Locate every malaria parasite and every leukocyte.
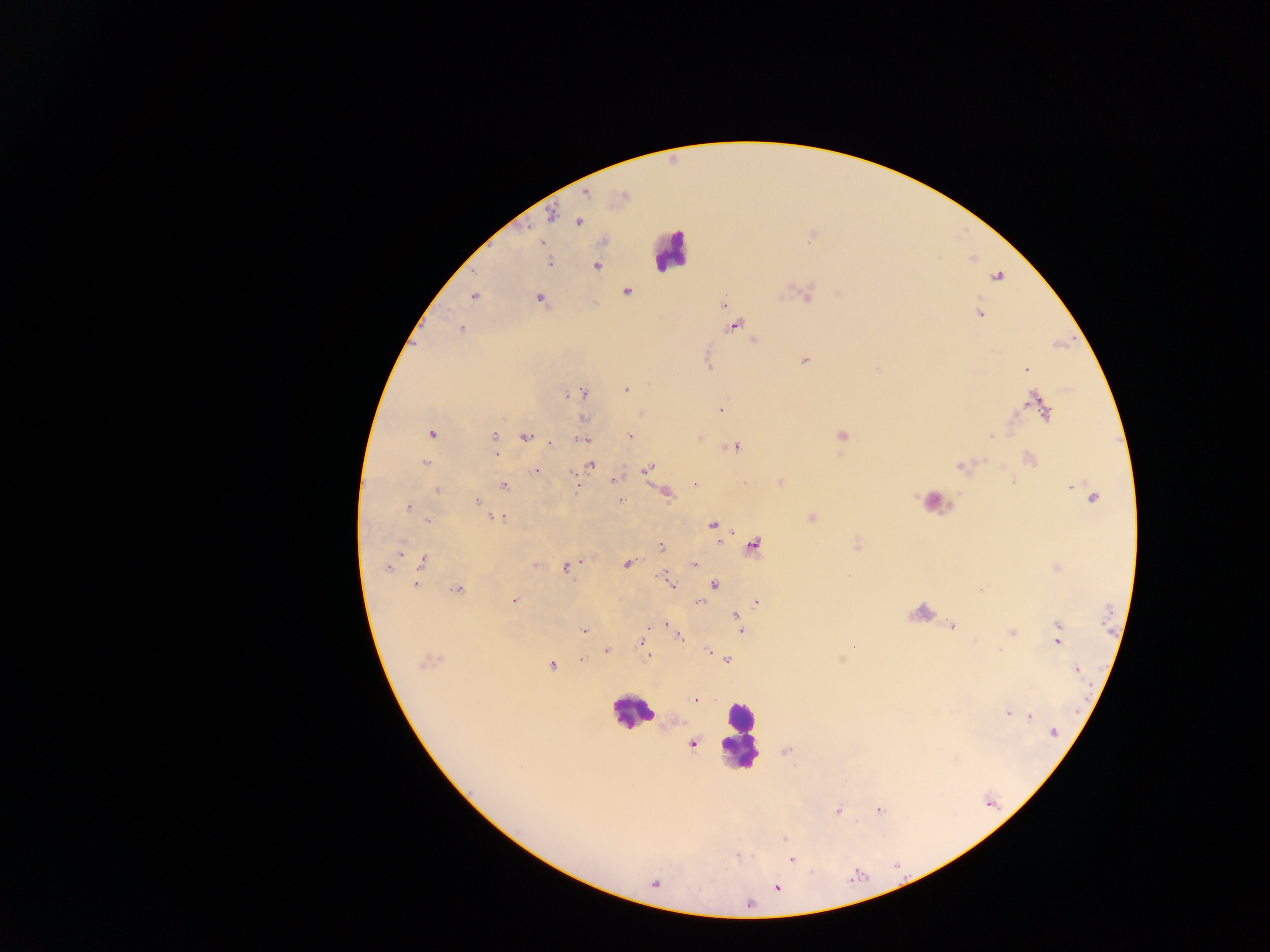

Approximate centers as [x, y] in pixels.
Malaria parasites: [585, 193], [621, 195], [550, 215], [578, 221], [812, 234], [541, 241], [549, 263], [595, 265], [997, 276], [626, 291], [806, 293], [473, 295], [539, 299], [723, 304], [728, 312], [978, 313], [734, 325], [461, 328], [753, 340], [804, 361], [709, 364], [1027, 369], [625, 390], [583, 392], [569, 393], [1041, 406], [720, 409], [640, 412], [582, 417], [432, 433], [493, 435], [631, 435], [840, 435], [990, 436], [525, 438], [700, 438], [582, 439], [551, 443], [733, 446], [495, 451], [1029, 459], [425, 463], [590, 464], [962, 465], [648, 469], [536, 471], [616, 480], [1012, 480], [780, 482], [576, 484], [695, 484], [1070, 484], [503, 486], [437, 490], [665, 493], [1092, 497], [477, 501], [621, 501], [408, 507], [499, 517], [812, 517], [427, 520], [712, 526], [752, 544], [856, 544], [660, 545], [398, 552], [422, 561], [581, 561], [627, 563], [694, 564], [535, 565], [387, 566], [566, 566], [1057, 567], [414, 584], [670, 585], [714, 585], [456, 589], [980, 590], [514, 600], [700, 601], [756, 601], [735, 616], [738, 619], [664, 623], [952, 625], [1057, 625], [669, 627], [582, 630], [740, 630], [1011, 631], [678, 636], [1057, 641], [641, 643], [853, 645], [606, 650], [709, 652], [645, 658], [727, 658], [581, 660], [428, 661], [551, 665], [1076, 670], [695, 700], [1008, 712], [1030, 716], [1053, 731], [691, 743], [785, 750], [878, 810], [838, 811], [783, 839], [790, 859], [653, 884], [776, 886].
Leukocytes: [671, 250], [932, 503], [632, 712], [738, 736].

Mobile-phone photograph taken through the microscope. Image is 1270×952 pixels. Sample from Ghana. Thick blood smear. Single field of view.